Report the malaria status of this cell.
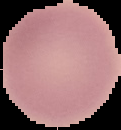

It is uninfected.

Summary:
  - Image type: segmented cell region with the area outside set to black
  - Image size: 121×130 pixels
  - Preparation: thin blood film